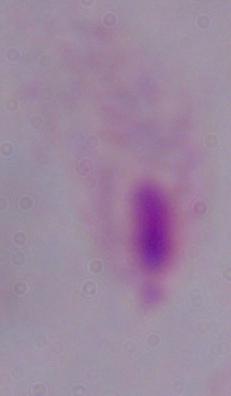
Summary:
  - Magnification: 1000x
  - Modality: photomicrograph
  - Identification: trichomonad